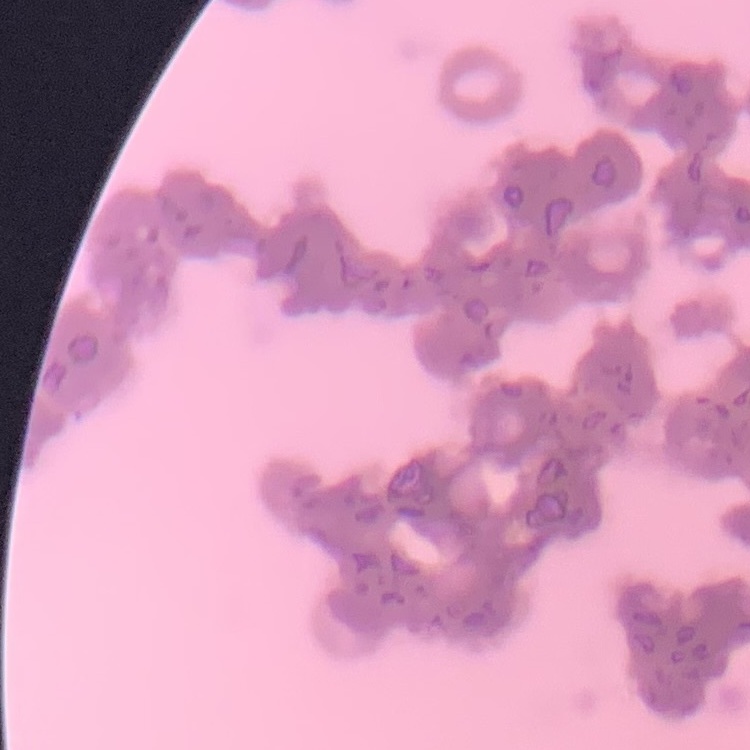

The erythrocytes exhibit rouleaux formation. Thin blood smear. One tile cut from a larger photomicrograph. Field's or Giemsa stain.